Report the malaria status of this cell.
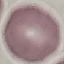
It is uninfected.

{
  "capture": "smartphone through the microscope eyepiece",
  "preparation": "thin smear",
  "image_type": "automatically extracted cell patch, resized to 64 × 64 pixels",
  "stain": "Giemsa"
}